Assess the morphology of the red blood cells.
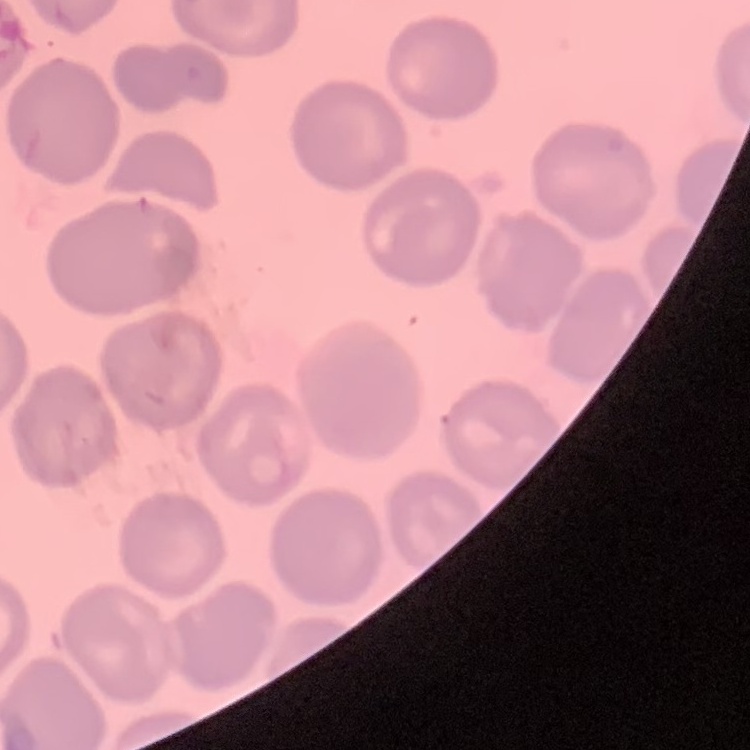

No rouleaux formation.

One tile cut from a larger photomicrograph. Stained with either Field's or Giemsa. Thin blood smear.